Describe the morphology of the red blood cells.
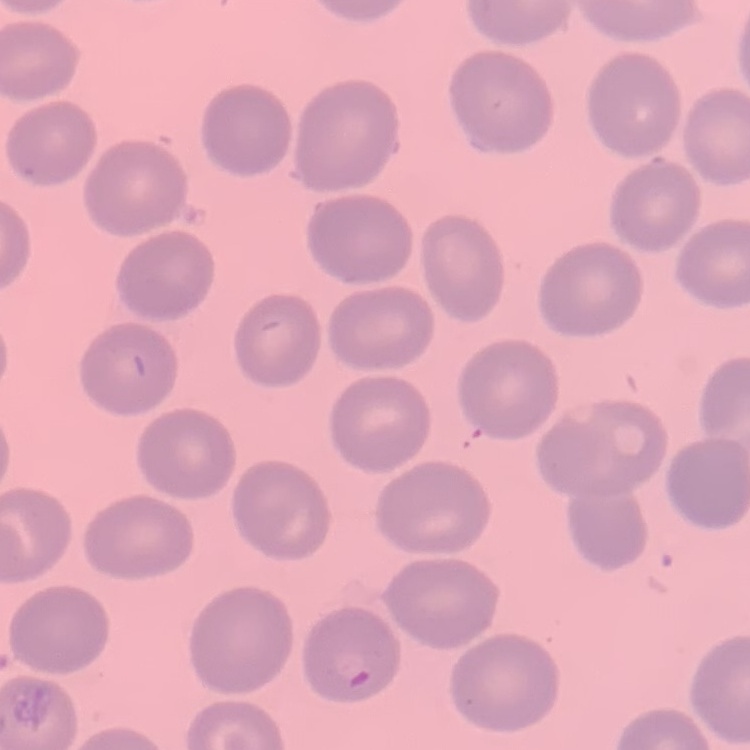
They show no rouleaux formation.

preparation = thin blood film
image type = square crop of a larger photomicrograph
stain = Field's or Giemsa